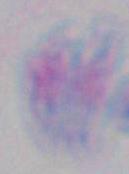
magnification = 1000x
modality = micrograph
identification = Toxoplasma gondii